Locate and identify every blood parasite.
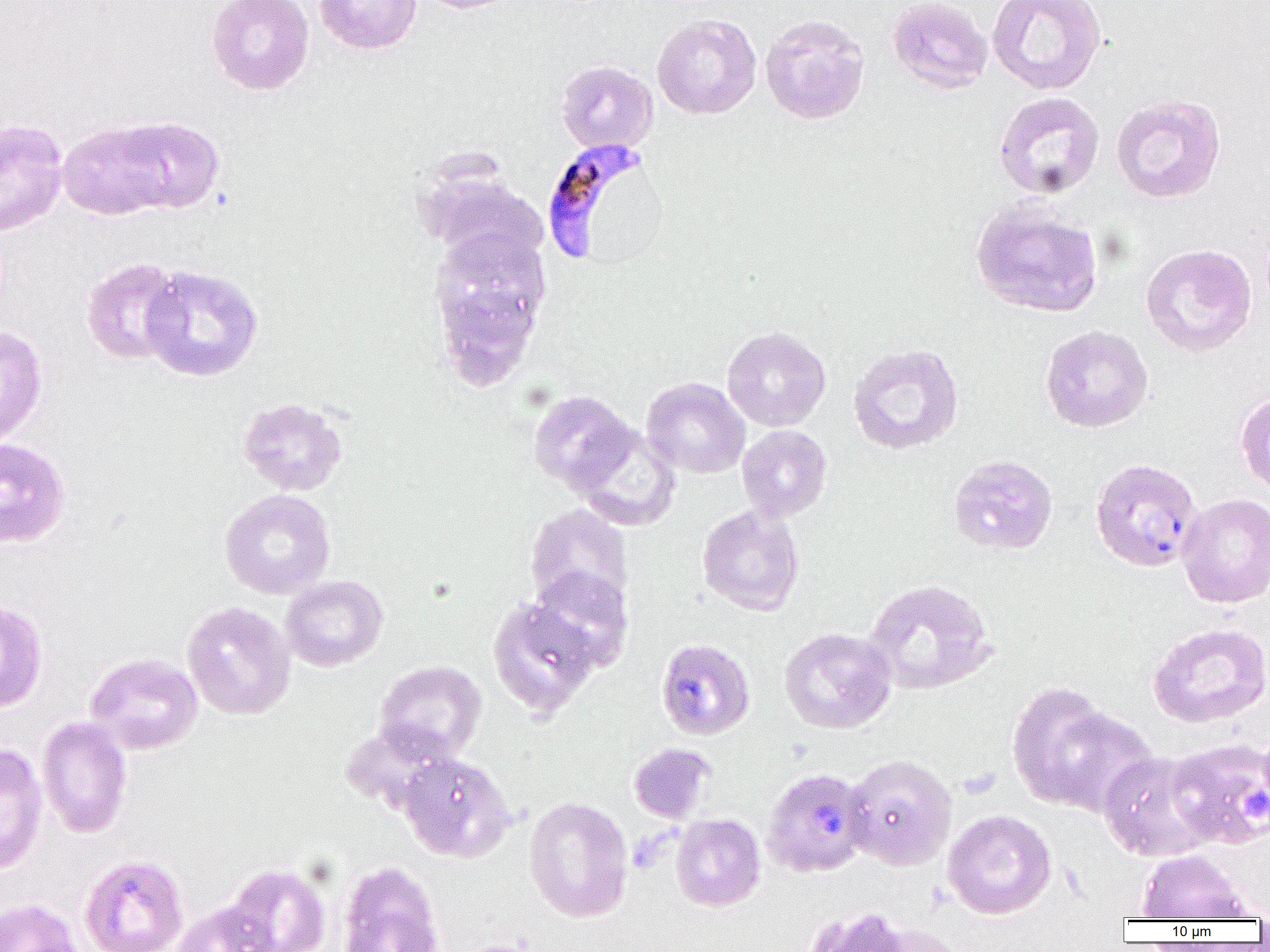

Approximate bounding boxes as (x1, y1, x2, y2) in pixels.
Plasmodium falciparum-infected red blood cells: (539, 138, 655, 266), (1089, 458, 1202, 572), (655, 638, 756, 741), (762, 767, 871, 878).
No Plasmodium ovale, Plasmodium malariae, Plasmodium vivax, Babesia divergens, or Trypanosoma brucei observed.

Summary:
  - Uninfected red blood cell locations: (206, 0, 315, 95), (315, 0, 422, 55), (413, 0, 525, 14), (887, 0, 993, 94), (987, 0, 1106, 95), (652, 13, 761, 119), (760, 14, 870, 125), (554, 60, 658, 154), (993, 91, 1105, 200), (1110, 93, 1226, 204), (110, 116, 224, 214), (0, 119, 68, 236), (57, 120, 174, 221), (415, 164, 546, 267), (970, 201, 1103, 318), (427, 225, 553, 377), (1140, 243, 1257, 357), (80, 257, 184, 365), (139, 264, 264, 382), (0, 325, 48, 447), (1040, 325, 1153, 433), (722, 326, 831, 431), (847, 342, 964, 455), (641, 377, 750, 479), (528, 390, 637, 493), (1235, 391, 1270, 498), (237, 396, 348, 496), (571, 424, 681, 531), (737, 425, 833, 521), (0, 437, 71, 548), (947, 454, 1059, 555), (220, 489, 335, 599), (1177, 493, 1270, 608), (696, 503, 805, 616), (525, 504, 634, 616), (528, 567, 634, 671), (280, 575, 388, 672), (863, 578, 997, 695), (488, 598, 600, 718), (0, 600, 49, 713), (182, 601, 296, 720), (1147, 622, 1270, 728), (779, 627, 897, 734), (85, 652, 203, 754), (374, 660, 487, 763), (1007, 681, 1129, 813), (37, 716, 133, 839), (1061, 724, 1189, 843), (1165, 737, 1270, 849), (0, 742, 48, 874), (628, 743, 715, 824), (1097, 750, 1220, 862), (397, 753, 516, 862), (844, 754, 958, 870), (525, 796, 633, 922), (942, 809, 1057, 920), (671, 813, 766, 911), (1135, 850, 1253, 921), (79, 853, 189, 952), (337, 861, 445, 952), (223, 863, 331, 952), (0, 898, 83, 952), (170, 900, 278, 952), (800, 904, 919, 952), (446, 939, 550, 952)
  - Platelet locations: (1234, 783, 1270, 831)
  - Slide-level diagnosis: Plasmodium falciparum
  - Preparation: thin blood film
  - Magnification: 1000x
  - Field of view: one of a larger specimen
  - Image size: 1270×952 pixels
  - Modality: optical microscopy